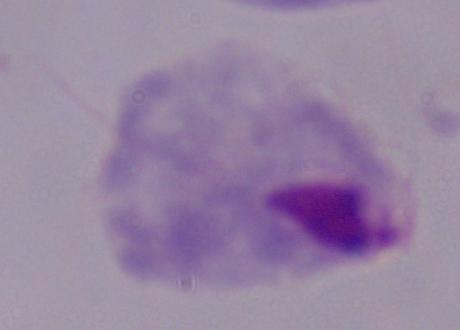

1000x magnification. A trichomonad is shown. Micrograph.